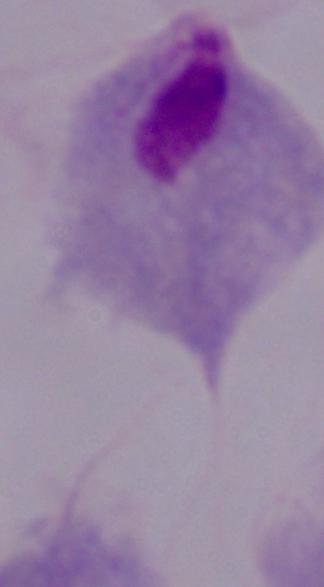

{
  "identification": "trichomonad",
  "magnification": "1000x",
  "modality": "micrograph"
}